State the preparation type.
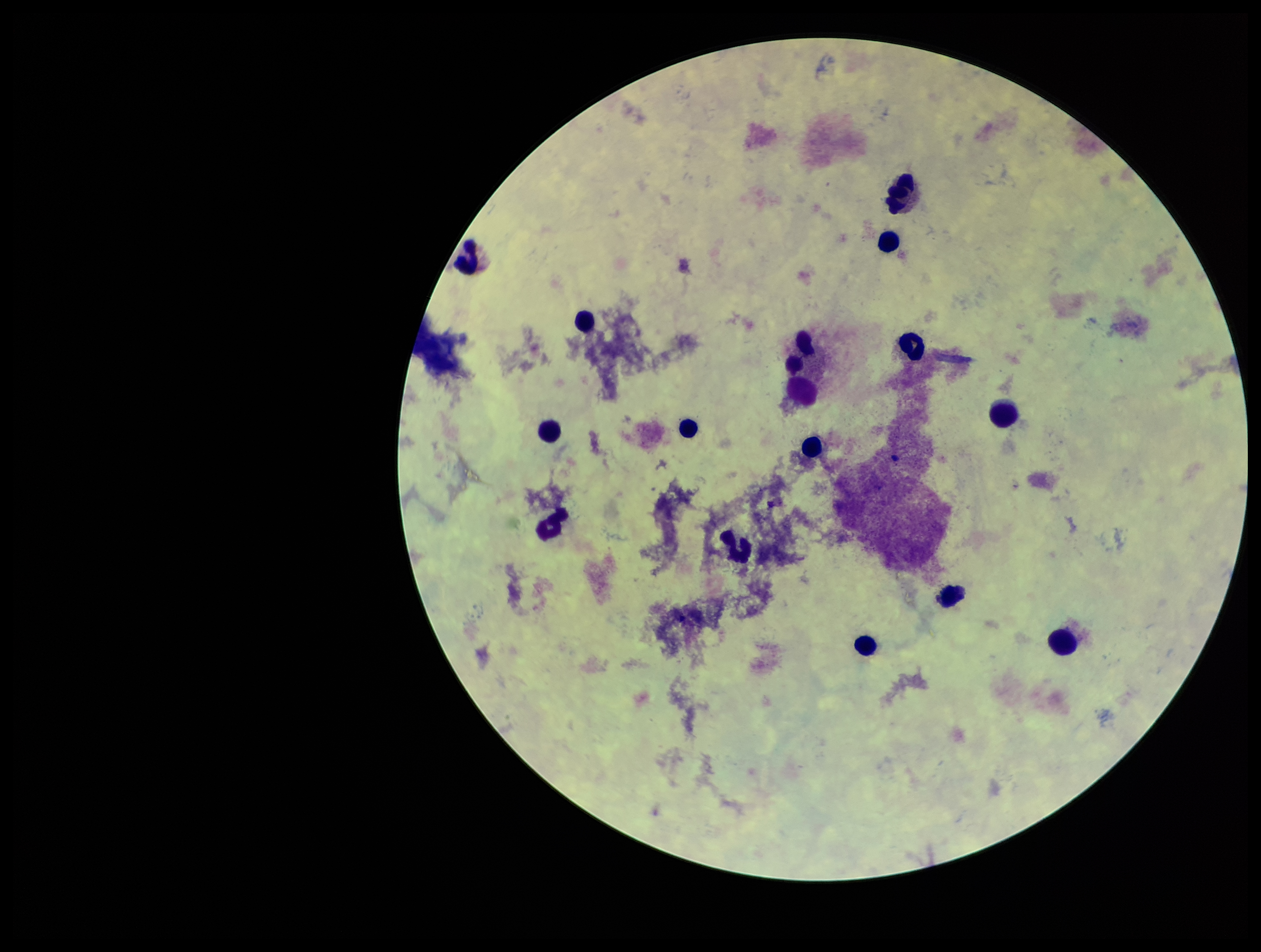

A thick smear.

Summary:
  - Stain: Giemsa
  - Capture: smartphone photograph through the microscope eyepiece
  - Parasite count: 0
  - Patient malaria status: negative
  - Plasmodium parasites: none identified
  - Leukocyte count: 16
  - Image size: 1261×952 pixels
  - Field of view: single